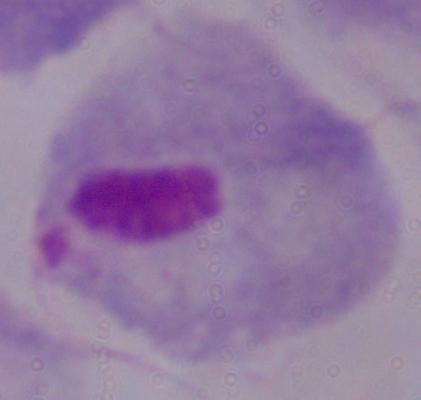
Summary:
  - Identification: trichomonad
  - Magnification: 1000x
  - Modality: photomicrograph